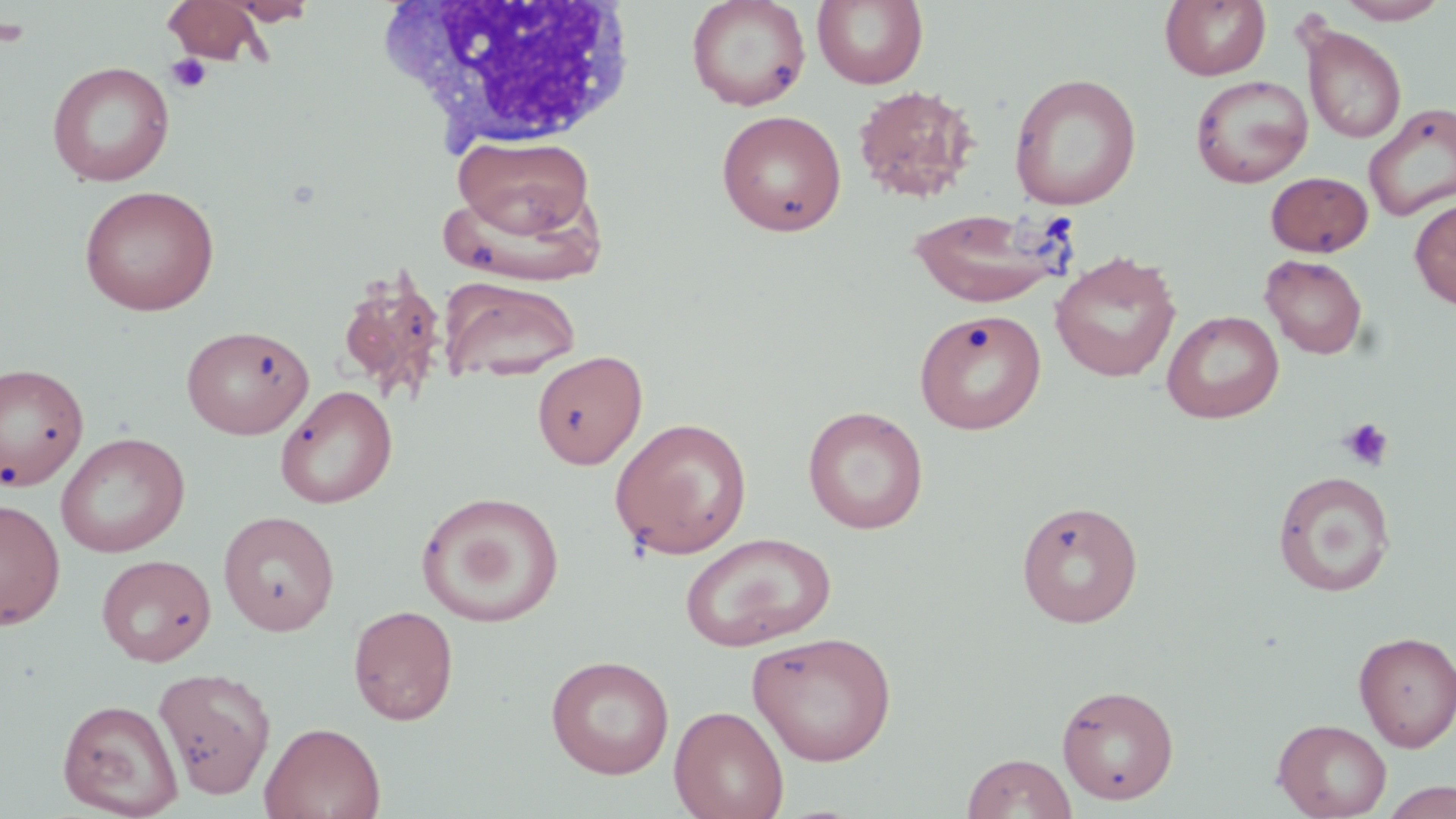
Approximate bounding boxes as named x1/y1/x2/y2 corners in pixels. Uninfected red blood cell locations: (x1=222, y1=0, x2=319, y2=25), (x1=686, y1=0, x2=811, y2=111), (x1=811, y1=0, x2=928, y2=89), (x1=1160, y1=0, x2=1271, y2=81), (x1=1336, y1=0, x2=1450, y2=24), (x1=164, y1=1, x2=272, y2=66), (x1=1301, y1=26, x2=1406, y2=144), (x1=46, y1=60, x2=175, y2=187), (x1=1009, y1=73, x2=1142, y2=210), (x1=1189, y1=74, x2=1314, y2=188), (x1=852, y1=83, x2=981, y2=203), (x1=1363, y1=104, x2=1456, y2=222), (x1=716, y1=109, x2=847, y2=236), (x1=454, y1=135, x2=594, y2=240), (x1=1265, y1=171, x2=1374, y2=257), (x1=78, y1=184, x2=220, y2=316), (x1=1410, y1=198, x2=1456, y2=311), (x1=908, y1=207, x2=1069, y2=308), (x1=1050, y1=251, x2=1181, y2=383), (x1=1260, y1=254, x2=1368, y2=359), (x1=336, y1=267, x2=448, y2=403), (x1=441, y1=277, x2=581, y2=383), (x1=1162, y1=310, x2=1284, y2=424), (x1=914, y1=311, x2=1047, y2=435), (x1=181, y1=324, x2=314, y2=439), (x1=532, y1=350, x2=648, y2=469), (x1=0, y1=361, x2=89, y2=492), (x1=275, y1=385, x2=397, y2=509), (x1=802, y1=405, x2=929, y2=534), (x1=609, y1=416, x2=753, y2=559), (x1=55, y1=432, x2=190, y2=557), (x1=1273, y1=471, x2=1397, y2=597), (x1=416, y1=491, x2=565, y2=627), (x1=0, y1=497, x2=66, y2=629), (x1=1016, y1=499, x2=1143, y2=628), (x1=218, y1=510, x2=341, y2=636), (x1=680, y1=532, x2=836, y2=652), (x1=96, y1=553, x2=216, y2=666), (x1=348, y1=605, x2=459, y2=725), (x1=746, y1=630, x2=897, y2=765), (x1=1354, y1=630, x2=1456, y2=750), (x1=546, y1=654, x2=674, y2=779), (x1=153, y1=666, x2=276, y2=798), (x1=1056, y1=683, x2=1179, y2=805), (x1=57, y1=698, x2=183, y2=817), (x1=669, y1=705, x2=790, y2=819), (x1=1273, y1=718, x2=1392, y2=818), (x1=260, y1=721, x2=386, y2=819), (x1=962, y1=752, x2=1077, y2=818), (x1=1379, y1=781, x2=1456, y2=819). Platelet locations: (x1=0, y1=16, x2=33, y2=47), (x1=165, y1=52, x2=212, y2=94), (x1=1338, y1=417, x2=1395, y2=472). White blood cell locations: (x1=384, y1=0, x2=642, y2=149). Slide-level diagnosis: no evidence of blood parasites. One field of a larger specimen. Light microscopy. Thin blood film. 1000x magnification. Image is 1456×819 pixels. May-Grünwald-Giemsa-stained preparation.